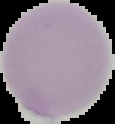

result = no Plasmodium parasites seen
image size = 115×124 pixels
image type = cell region segmented out of the field of view; surrounding area masked to black
preparation = thin blood film